Outline each Plasmodium ovale-infected red blood cell.
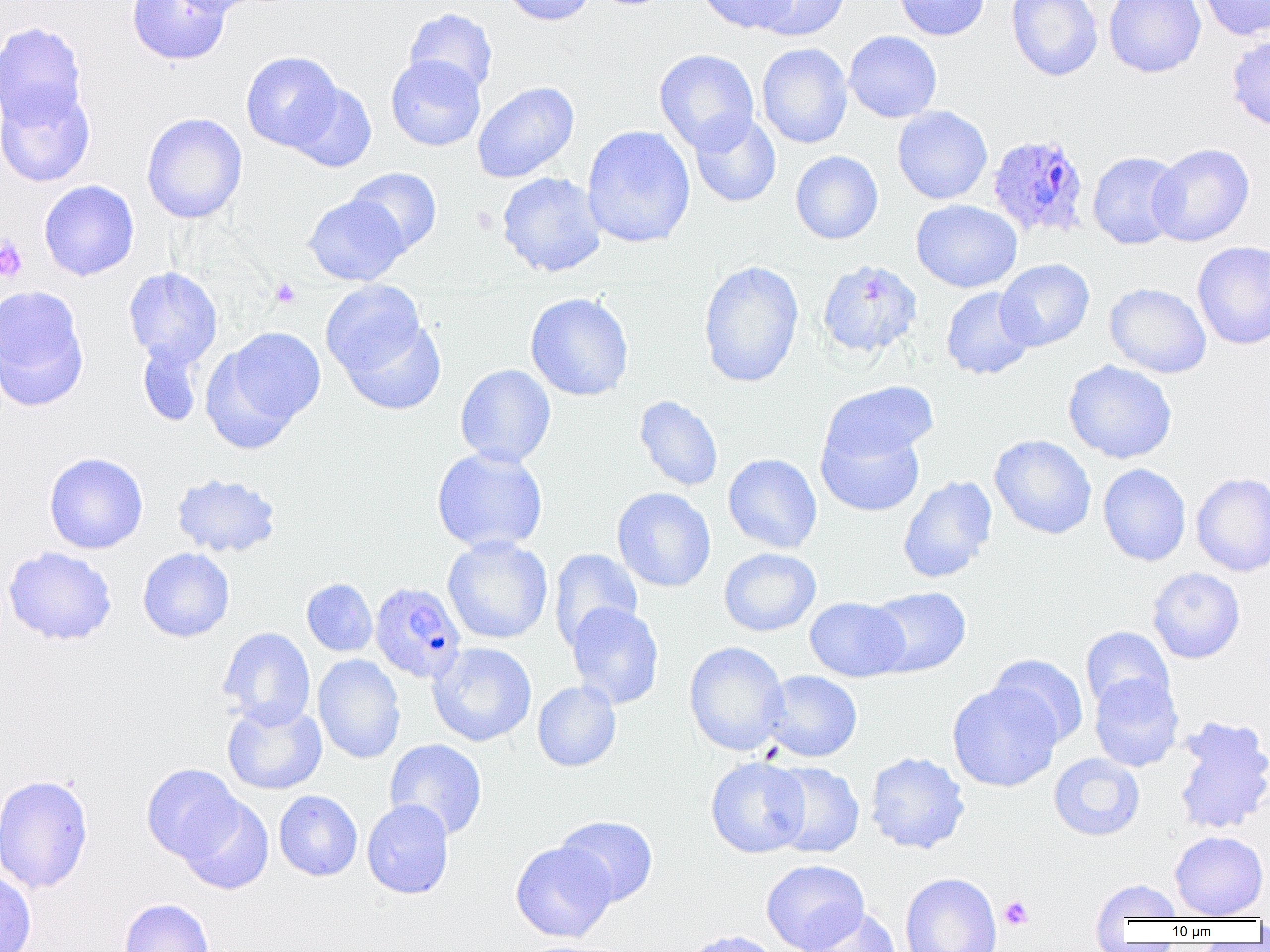

Approximate bounding boxes as (x1, y1, x2, y2) in pixels.
Plasmodium ovale-infected red blood cells: (986, 133, 1090, 240), (373, 581, 470, 684).

{
  "slide_level_diagnosis": "Plasmodium ovale",
  "platelet_locations": "approximate bounding boxes as (x1, y1, x2, y2) in pixels: (0, 238, 28, 282), (270, 277, 301, 309), (999, 896, 1034, 931)",
  "preparation": "thin blood film",
  "magnification": "1000x",
  "image_size": "1270×952 pixels",
  "uninfected_red_blood_cell_locations": "approximate bounding boxes as (x1, y1, x2, y2) in pixels: (127, 0, 230, 65), (168, 0, 265, 16), (501, 0, 596, 25), (696, 0, 798, 34), (750, 0, 851, 41), (893, 0, 990, 41), (1006, 0, 1103, 81), (1104, 0, 1206, 78), (1197, 0, 1270, 41), (404, 8, 497, 95), (0, 22, 88, 127), (844, 30, 942, 122), (1226, 33, 1270, 133), (757, 43, 852, 149), (654, 48, 759, 154), (241, 51, 343, 152), (386, 55, 486, 151), (285, 81, 376, 172), (472, 81, 579, 183), (0, 82, 96, 187), (893, 106, 992, 205), (689, 112, 781, 208), (142, 113, 247, 223), (582, 125, 696, 249), (1148, 143, 1254, 247), (790, 150, 883, 244), (1087, 150, 1185, 250), (346, 167, 442, 256), (496, 172, 607, 277), (39, 180, 140, 281), (303, 195, 408, 285), (911, 199, 1022, 293), (1192, 241, 1270, 350), (995, 258, 1095, 351), (698, 260, 804, 388), (818, 260, 922, 359), (123, 267, 223, 368), (320, 279, 431, 379), (1104, 282, 1212, 379), (0, 285, 89, 410), (940, 286, 1036, 380), (525, 292, 633, 401), (337, 314, 446, 415), (207, 327, 326, 446), (137, 339, 206, 427), (1063, 360, 1177, 464), (455, 364, 556, 467), (821, 380, 939, 467), (634, 395, 724, 492), (816, 420, 926, 519), (989, 434, 1097, 539), (431, 447, 548, 555), (43, 452, 148, 554), (723, 453, 822, 554), (1098, 463, 1191, 566), (1190, 472, 1270, 577), (171, 473, 282, 558), (898, 476, 997, 583), (612, 487, 716, 592), (442, 536, 553, 644), (3, 546, 117, 646), (138, 547, 235, 642), (718, 547, 821, 636), (548, 548, 643, 650), (1148, 567, 1245, 664), (301, 578, 377, 656), (865, 586, 972, 678), (804, 597, 909, 682), (566, 603, 664, 709), (1080, 626, 1175, 715), (218, 627, 315, 728), (684, 641, 790, 756), (428, 642, 537, 747), (313, 654, 405, 764), (989, 654, 1089, 748), (760, 670, 863, 762), (1089, 672, 1184, 772), (532, 681, 621, 771), (947, 682, 1062, 792), (222, 700, 327, 795), (1170, 715, 1270, 836), (384, 738, 487, 841), (865, 752, 970, 854), (1048, 752, 1145, 841), (705, 756, 810, 858), (767, 761, 864, 858), (141, 763, 243, 864), (0, 774, 93, 894), (274, 790, 362, 881), (177, 794, 274, 895), (362, 799, 454, 899), (555, 815, 658, 906), (1169, 831, 1268, 919), (510, 841, 616, 942), (761, 859, 869, 952), (0, 868, 37, 952), (900, 872, 1002, 952), (1090, 877, 1183, 925), (119, 898, 214, 952), (800, 907, 902, 952), (681, 930, 783, 952), (515, 939, 634, 952)",
  "modality": "light microscopy",
  "field_of_view": "one of a larger specimen"
}